Describe the morphology of the erythrocytes.
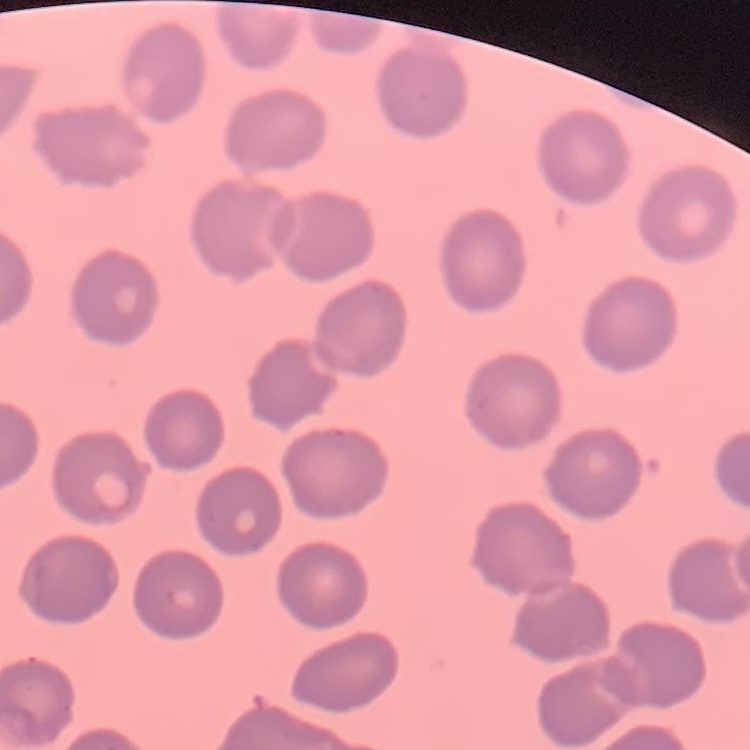

They show no rouleaux formation.

Thin blood film. Stained with either Field's or Giemsa. Square crop of a larger photomicrograph.